Locate every Trypanosoma brucei.
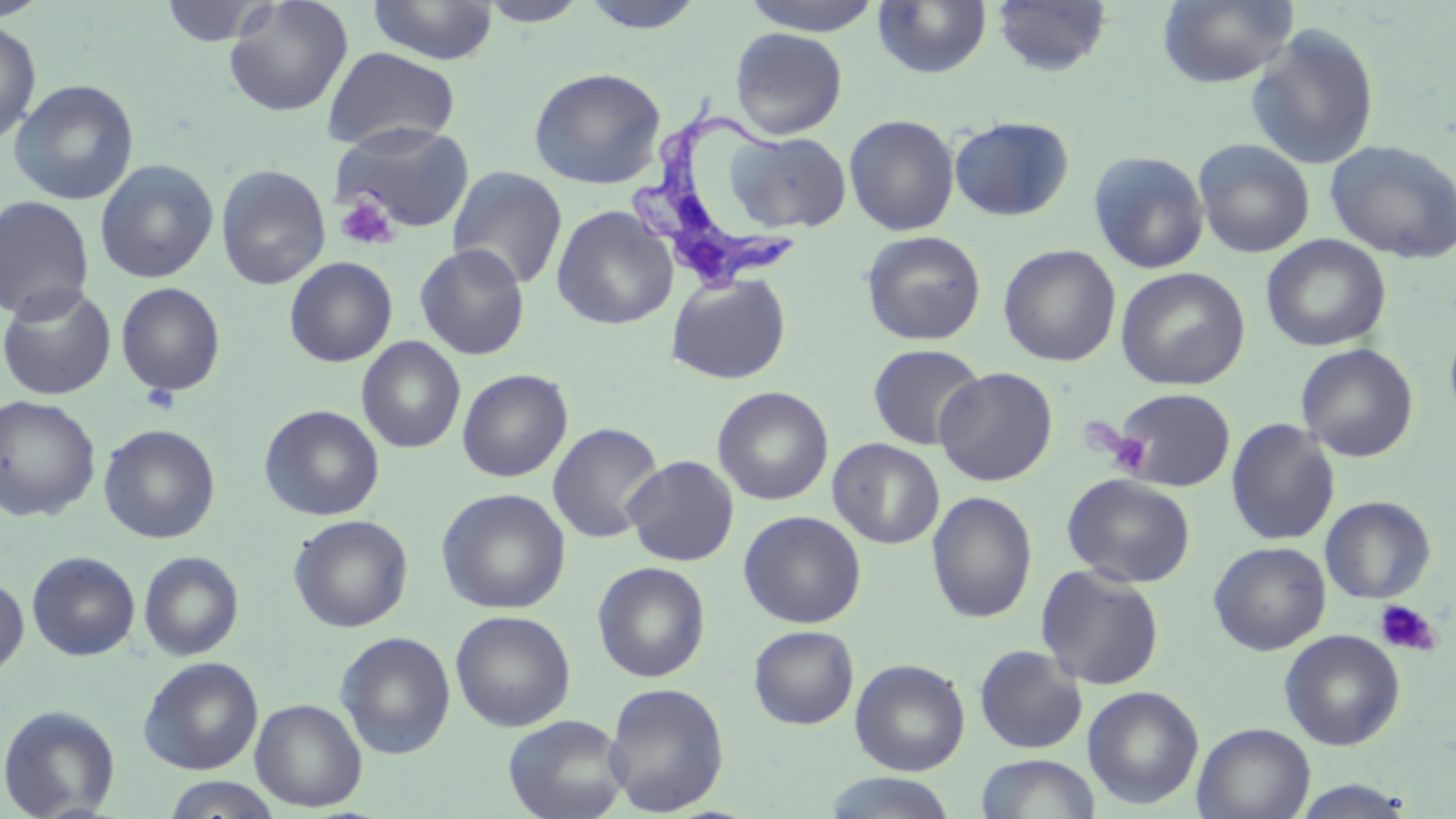

Approximate bounding boxes as named x1/y1/x2/y2 corners in pixels.
Trypanosoma brucei: (x1=625, y1=104, x2=814, y2=296).

slide_level_diagnosis: Trypanosoma brucei
uninfected_red_blood_cell_locations: 'approximate bounding boxes as named x1/y1/x2/y2 corners in pixels: (x1=157, y1=0, x2=278, y2=48), (x1=222, y1=0, x2=353, y2=117), (x1=579, y1=0, x2=707, y2=34), (x1=741, y1=0, x2=883, y2=36), (x1=1158, y1=0, x2=1299, y2=88), (x1=368, y1=1, x2=499, y2=65), (x1=477, y1=1, x2=590, y2=26), (x1=873, y1=1, x2=992, y2=79), (x1=990, y1=1, x2=1114, y2=77), (x1=0, y1=20, x2=41, y2=146), (x1=1245, y1=24, x2=1381, y2=170), (x1=730, y1=27, x2=847, y2=140), (x1=322, y1=46, x2=461, y2=152), (x1=528, y1=67, x2=667, y2=189), (x1=9, y1=78, x2=139, y2=206), (x1=843, y1=114, x2=960, y2=236), (x1=949, y1=116, x2=1074, y2=221), (x1=333, y1=122, x2=476, y2=232), (x1=729, y1=131, x2=853, y2=234), (x1=1193, y1=138, x2=1315, y2=258), (x1=1325, y1=140, x2=1456, y2=264), (x1=1088, y1=150, x2=1210, y2=274), (x1=95, y1=159, x2=218, y2=283), (x1=216, y1=164, x2=331, y2=290), (x1=447, y1=166, x2=568, y2=291), (x1=0, y1=196, x2=95, y2=322), (x1=551, y1=205, x2=679, y2=329), (x1=861, y1=230, x2=986, y2=345), (x1=1261, y1=235, x2=1391, y2=352), (x1=414, y1=243, x2=531, y2=360), (x1=998, y1=245, x2=1121, y2=367), (x1=995, y1=256, x2=1249, y2=373), (x1=284, y1=257, x2=398, y2=367), (x1=1116, y1=267, x2=1251, y2=391), (x1=666, y1=272, x2=791, y2=384), (x1=116, y1=282, x2=225, y2=396), (x1=0, y1=284, x2=117, y2=400), (x1=356, y1=336, x2=467, y2=453), (x1=867, y1=343, x2=986, y2=450), (x1=1296, y1=343, x2=1418, y2=462), (x1=934, y1=367, x2=1058, y2=487), (x1=457, y1=368, x2=573, y2=482), (x1=713, y1=386, x2=833, y2=506), (x1=1110, y1=388, x2=1237, y2=491), (x1=0, y1=395, x2=101, y2=522), (x1=259, y1=404, x2=385, y2=521), (x1=1226, y1=418, x2=1341, y2=546), (x1=547, y1=422, x2=664, y2=543), (x1=98, y1=424, x2=221, y2=544), (x1=828, y1=438, x2=944, y2=549), (x1=622, y1=455, x2=740, y2=566), (x1=1062, y1=473, x2=1196, y2=588), (x1=436, y1=488, x2=571, y2=614), (x1=927, y1=491, x2=1038, y2=624), (x1=1320, y1=496, x2=1436, y2=604), (x1=738, y1=510, x2=866, y2=628), (x1=288, y1=514, x2=413, y2=633), (x1=1208, y1=541, x2=1331, y2=655), (x1=26, y1=551, x2=141, y2=661), (x1=138, y1=551, x2=244, y2=661), (x1=591, y1=561, x2=711, y2=682), (x1=1036, y1=565, x2=1165, y2=690), (x1=0, y1=574, x2=29, y2=679), (x1=1247, y1=580, x2=1402, y2=699), (x1=450, y1=610, x2=576, y2=732), (x1=749, y1=625, x2=859, y2=730), (x1=1279, y1=629, x2=1405, y2=750), (x1=336, y1=631, x2=456, y2=759), (x1=974, y1=645, x2=1088, y2=754), (x1=138, y1=656, x2=263, y2=775), (x1=850, y1=658, x2=970, y2=776), (x1=603, y1=681, x2=730, y2=816), (x1=1082, y1=686, x2=1204, y2=810), (x1=250, y1=698, x2=367, y2=812), (x1=0, y1=704, x2=121, y2=818), (x1=503, y1=714, x2=630, y2=819), (x1=1192, y1=722, x2=1315, y2=819), (x1=975, y1=753, x2=1100, y2=819), (x1=820, y1=772, x2=959, y2=818), (x1=162, y1=776, x2=282, y2=818), (x1=1289, y1=780, x2=1419, y2=818)'
modality: light microscopy
image_size: 1456×819 pixels
field_of_view: one of a larger specimen
magnification: 1000x
preparation: thin blood film
stain: May-Grünwald-Giemsa
platelet_locations: 'approximate bounding boxes as named x1/y1/x2/y2 corners in pixels: (x1=335, y1=195, x2=399, y2=251), (x1=141, y1=383, x2=180, y2=415), (x1=1105, y1=429, x2=1155, y2=478), (x1=1373, y1=598, x2=1441, y2=658)'